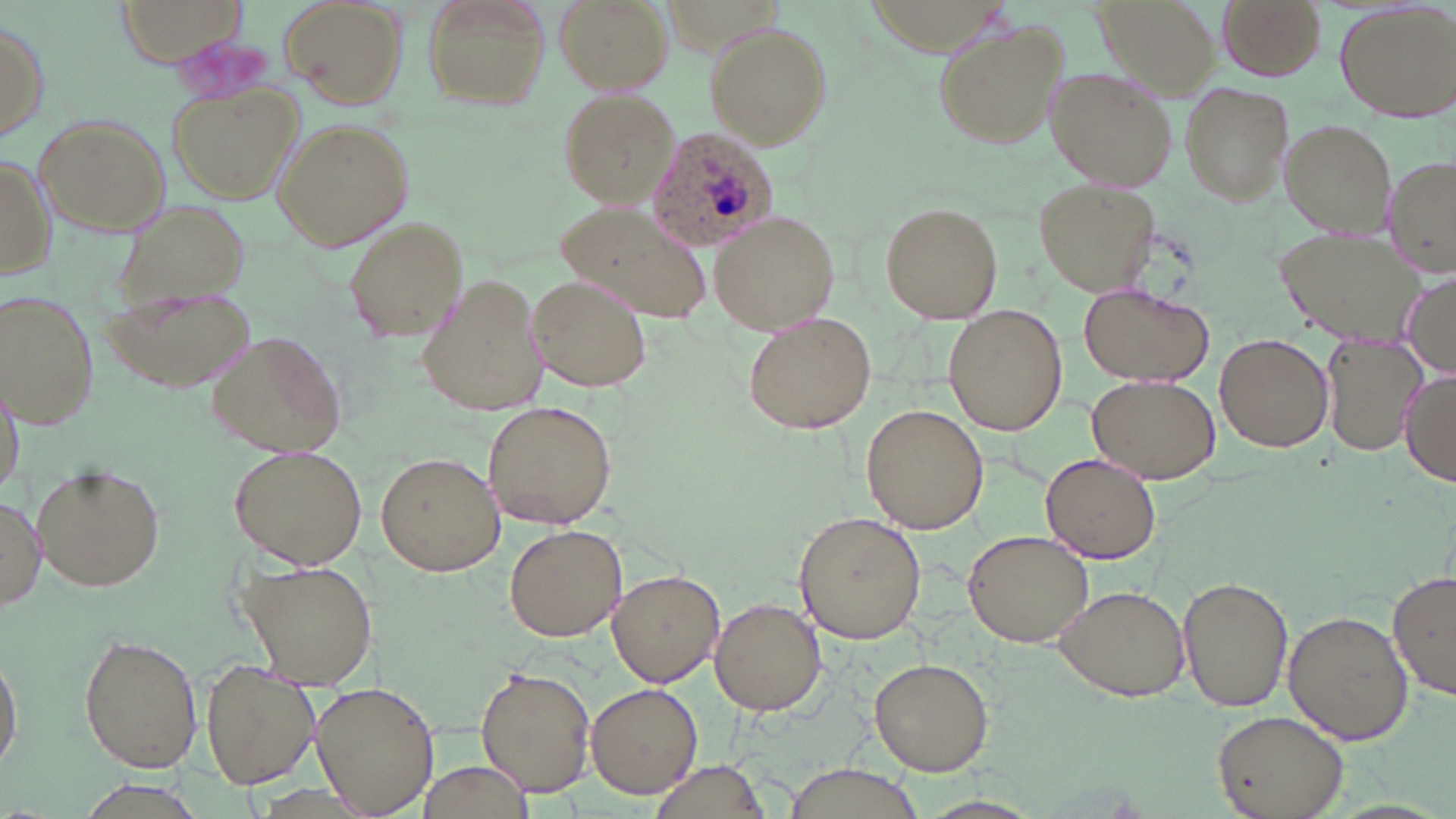
Approximate bounding boxes as named x1/y1/x2/y2 corners in pixels. Uninfected red blood cell locations: (x1=114, y1=0, x2=251, y2=68), (x1=278, y1=0, x2=408, y2=109), (x1=423, y1=0, x2=549, y2=115), (x1=554, y1=0, x2=674, y2=93), (x1=1216, y1=0, x2=1325, y2=80), (x1=1335, y1=0, x2=1455, y2=121), (x1=1091, y1=1, x2=1221, y2=96), (x1=1, y1=14, x2=49, y2=148), (x1=931, y1=20, x2=1066, y2=150), (x1=705, y1=23, x2=830, y2=146), (x1=1045, y1=65, x2=1176, y2=190), (x1=1179, y1=82, x2=1293, y2=209), (x1=168, y1=83, x2=303, y2=206), (x1=557, y1=88, x2=680, y2=206), (x1=33, y1=112, x2=171, y2=240), (x1=273, y1=117, x2=413, y2=251), (x1=1280, y1=119, x2=1394, y2=240), (x1=0, y1=151, x2=53, y2=280), (x1=1384, y1=157, x2=1456, y2=278), (x1=1036, y1=179, x2=1163, y2=296), (x1=880, y1=202, x2=1001, y2=322), (x1=551, y1=203, x2=712, y2=324), (x1=711, y1=209, x2=842, y2=334), (x1=343, y1=216, x2=468, y2=342), (x1=1282, y1=227, x2=1428, y2=347), (x1=415, y1=271, x2=555, y2=418), (x1=1399, y1=273, x2=1456, y2=374), (x1=527, y1=274, x2=653, y2=392), (x1=103, y1=283, x2=257, y2=392), (x1=1078, y1=285, x2=1214, y2=387), (x1=2, y1=288, x2=101, y2=430), (x1=946, y1=306, x2=1068, y2=434), (x1=742, y1=312, x2=877, y2=434), (x1=205, y1=330, x2=348, y2=459), (x1=1215, y1=333, x2=1334, y2=453), (x1=1321, y1=335, x2=1425, y2=456), (x1=1398, y1=367, x2=1456, y2=484), (x1=0, y1=373, x2=26, y2=497), (x1=1087, y1=375, x2=1222, y2=484), (x1=482, y1=400, x2=618, y2=530), (x1=861, y1=405, x2=988, y2=535), (x1=229, y1=445, x2=367, y2=570), (x1=375, y1=452, x2=505, y2=576), (x1=1041, y1=453, x2=1161, y2=564), (x1=34, y1=462, x2=165, y2=592), (x1=0, y1=491, x2=46, y2=612), (x1=793, y1=510, x2=926, y2=644), (x1=504, y1=523, x2=627, y2=642), (x1=963, y1=528, x2=1097, y2=646), (x1=239, y1=556, x2=381, y2=688), (x1=607, y1=570, x2=725, y2=687), (x1=1389, y1=571, x2=1456, y2=702), (x1=1178, y1=574, x2=1293, y2=713), (x1=1052, y1=584, x2=1190, y2=701), (x1=710, y1=597, x2=826, y2=716), (x1=1283, y1=610, x2=1413, y2=745), (x1=79, y1=633, x2=202, y2=773), (x1=0, y1=640, x2=26, y2=776), (x1=869, y1=656, x2=995, y2=776), (x1=200, y1=659, x2=319, y2=791), (x1=475, y1=666, x2=597, y2=796), (x1=587, y1=683, x2=703, y2=799), (x1=309, y1=684, x2=439, y2=814), (x1=1212, y1=710, x2=1349, y2=819), (x1=411, y1=758, x2=538, y2=819), (x1=650, y1=761, x2=773, y2=819), (x1=784, y1=765, x2=927, y2=817). Plasmodium ovale-infected red blood cell locations: (x1=648, y1=126, x2=779, y2=250). Slide-level diagnosis: Plasmodium ovale. Image is 1456×819 pixels. One field of a larger specimen. Optical microscopy. Thin blood film. 1000x magnification. May-Grünwald-Giemsa-stained preparation.